Name the blood parasite species.
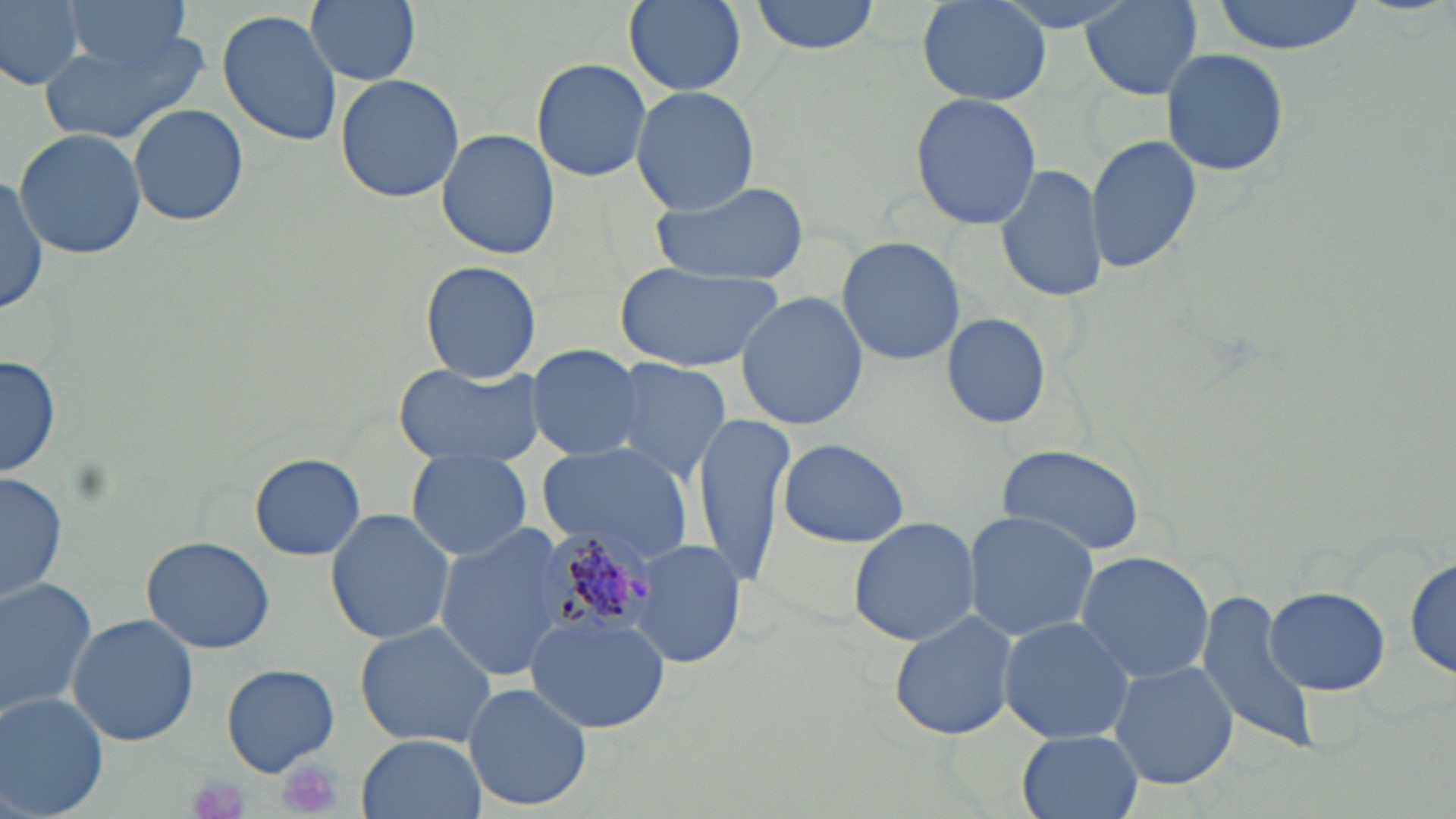
Plasmodium malariae.

Approximate bounding boxes as [x1, y1, x2, y2] in pixels. Plasmodium malariae-infected red blood cell locations: [536, 523, 660, 642]. Uninfected red blood cell locations: [1, 0, 86, 91], [57, 0, 196, 69], [305, 0, 421, 87], [752, 0, 881, 55], [992, 0, 1145, 32], [1210, 0, 1365, 54], [623, 1, 747, 96], [918, 1, 1051, 107], [1079, 1, 1204, 100], [218, 8, 344, 147], [41, 29, 212, 148], [1161, 48, 1290, 177], [530, 56, 652, 181], [334, 73, 465, 204], [631, 87, 760, 215], [910, 93, 1042, 230], [129, 105, 247, 225], [14, 128, 146, 259], [437, 130, 559, 259], [1085, 131, 1202, 275], [994, 165, 1107, 303], [0, 169, 49, 320], [649, 177, 811, 284], [837, 236, 965, 365], [420, 261, 543, 385], [617, 261, 785, 374], [735, 291, 868, 431], [942, 312, 1051, 429], [526, 344, 644, 460], [1, 354, 60, 479], [608, 357, 734, 482], [393, 361, 545, 467], [693, 414, 796, 584], [776, 437, 911, 548], [539, 441, 698, 567], [998, 442, 1148, 554], [408, 448, 533, 562], [250, 452, 365, 560], [2, 471, 68, 606], [325, 508, 453, 646], [962, 511, 1098, 643], [846, 516, 982, 646], [433, 525, 572, 681], [141, 537, 277, 654], [630, 538, 744, 669], [1405, 550, 1454, 680], [1073, 551, 1214, 684], [0, 577, 100, 722], [1263, 585, 1389, 694], [1195, 589, 1320, 758], [889, 608, 1019, 742], [526, 611, 671, 732], [67, 614, 198, 746], [998, 616, 1136, 746], [353, 621, 499, 753], [1107, 658, 1240, 791], [223, 664, 341, 777], [464, 681, 592, 812], [0, 694, 109, 819], [1017, 730, 1143, 819], [357, 733, 483, 819]. Platelet locations: [274, 755, 344, 817], [188, 773, 251, 817]. May-Grünwald-Giemsa stain. 1000x magnification. Image is 1456×819 pixels. Optical microscopy. Thin blood film. Single field of view.